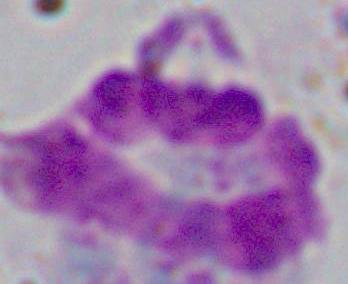

Summary:
  - Modality: photomicrograph
  - Magnification: 1000x
  - Identification: white blood cell